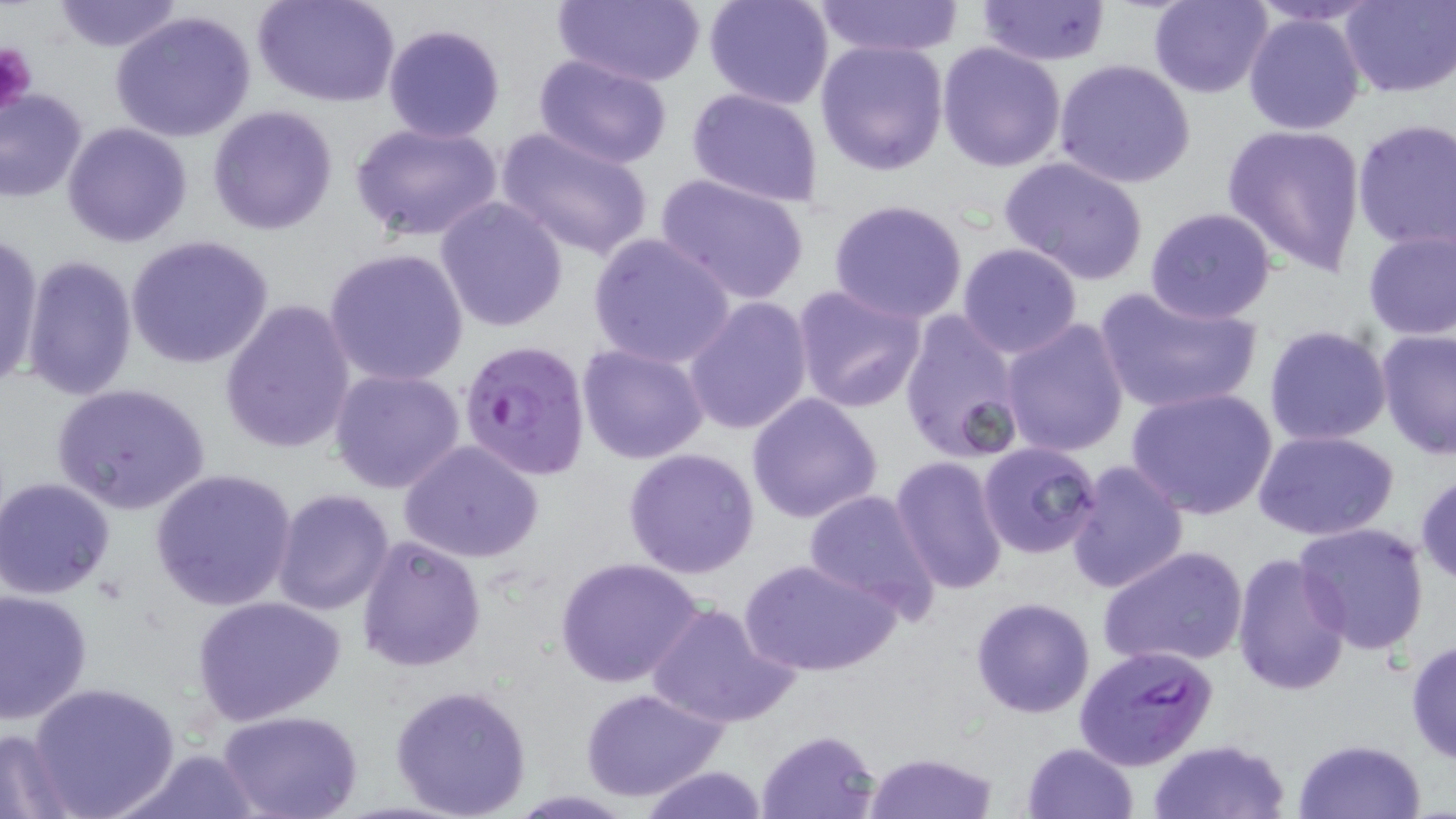
Approximate bounding boxes as (x1, y1, x2, y2) in pixels. Platelet locations: (0, 40, 39, 118). Uninfected red blood cell locations: (50, 0, 185, 53), (254, 0, 401, 108), (551, 0, 708, 88), (703, 0, 836, 111), (1149, 0, 1274, 99), (1243, 0, 1386, 26), (1338, 0, 1456, 99), (813, 1, 965, 56), (977, 1, 1112, 66), (110, 10, 259, 143), (1242, 12, 1366, 136), (382, 23, 506, 142), (815, 39, 950, 176), (937, 41, 1067, 173), (533, 54, 675, 168), (1053, 59, 1197, 191), (685, 88, 825, 206), (0, 89, 89, 203), (208, 105, 338, 235), (1351, 120, 1456, 252), (63, 121, 193, 247), (350, 121, 503, 245), (1221, 122, 1368, 275), (493, 126, 655, 265), (999, 156, 1150, 285), (655, 173, 810, 305), (434, 196, 569, 335), (828, 198, 969, 323), (1143, 206, 1278, 324), (1360, 227, 1456, 342), (587, 232, 737, 371), (0, 233, 43, 391), (125, 234, 274, 369), (956, 241, 1085, 358), (324, 247, 470, 387), (22, 254, 139, 403), (792, 285, 928, 413), (1092, 286, 1263, 417), (683, 295, 814, 435), (218, 299, 358, 455), (899, 308, 1026, 464), (1001, 317, 1130, 457), (1263, 323, 1393, 448), (1375, 329, 1456, 459), (577, 344, 710, 464), (328, 369, 466, 493), (51, 382, 212, 515), (1125, 385, 1279, 521), (745, 392, 883, 523), (1253, 429, 1399, 540), (399, 441, 545, 563), (978, 442, 1101, 559), (623, 448, 762, 579), (890, 456, 1009, 596), (1062, 459, 1188, 596), (150, 469, 300, 613), (1414, 472, 1456, 587), (0, 476, 117, 599), (272, 489, 396, 614), (803, 489, 940, 618), (1292, 522, 1431, 654), (356, 533, 488, 671), (1098, 544, 1250, 669), (1230, 553, 1352, 697), (556, 557, 705, 688), (741, 558, 899, 678), (0, 588, 94, 725), (193, 595, 345, 726), (970, 597, 1095, 718), (644, 601, 799, 730), (1406, 637, 1456, 766), (26, 679, 180, 819), (389, 682, 532, 818), (580, 687, 728, 802), (219, 710, 364, 819), (0, 727, 78, 817), (756, 729, 881, 817), (1147, 739, 1292, 819), (1292, 739, 1426, 819), (1021, 741, 1139, 818), (113, 747, 263, 818), (863, 750, 999, 819), (639, 764, 769, 819). Plasmodium falciparum-infected red blood cell locations: (458, 341, 592, 481), (1074, 642, 1220, 771). Slide-level diagnosis: Plasmodium falciparum. May-Grünwald-Giemsa stain. 1000x magnification. Optical microscopy. Thin blood smear. Image is 1456×819 pixels. One field of a larger specimen.